Assess this cell for malaria.
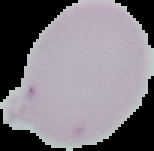

Uninfected.

Image is 154×151 pixels. Cell region segmented out of the field of view; the surrounding area is masked to black. From a thin blood film.